Name the parasite shown.
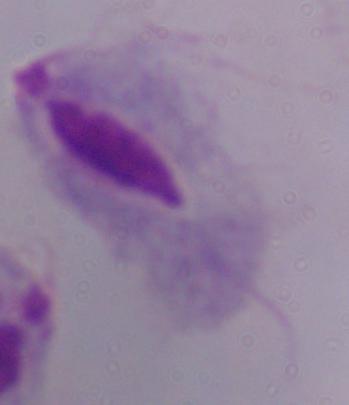
This is a trichomonad.

Photomicrograph. Captured at 1000x magnification.